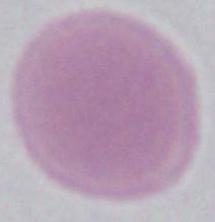
modality: micrograph
identification: erythrocyte
magnification: 1000x